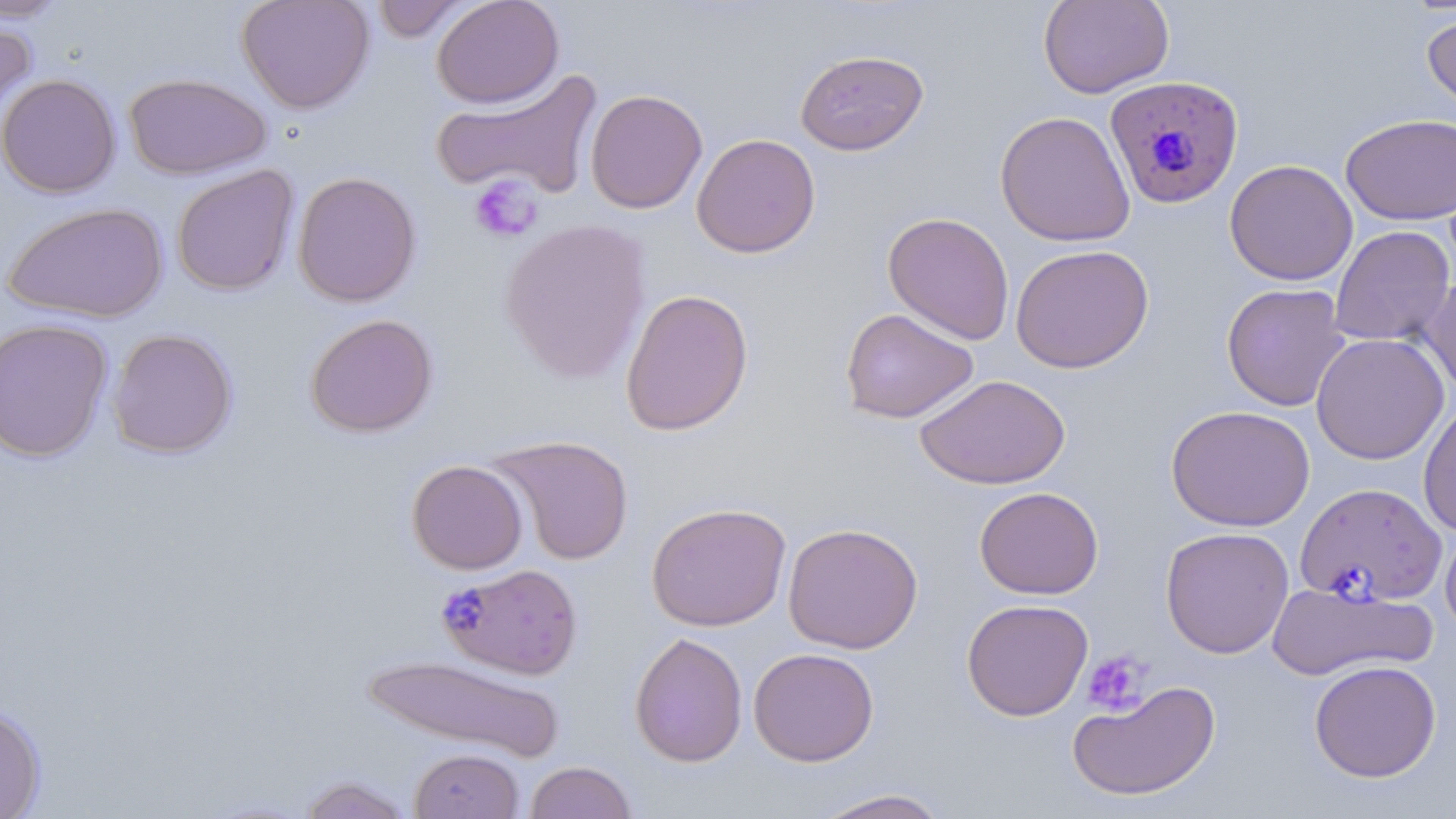
Approximate bounding boxes as (x1, y1, x2, y2) in pixels. Plasmodium falciparum-infected red blood cell locations: (1104, 75, 1244, 210), (1295, 481, 1447, 605), (437, 569, 579, 684). Platelet locations: (469, 173, 544, 244), (1082, 650, 1152, 716). Uninfected red blood cell locations: (0, 0, 71, 22), (237, 0, 375, 114), (370, 0, 473, 42), (431, 0, 564, 109), (1038, 0, 1174, 99), (1421, 11, 1456, 118), (0, 14, 37, 131), (795, 49, 929, 156), (432, 70, 603, 201), (123, 72, 272, 180), (0, 74, 121, 198), (585, 89, 708, 214), (994, 110, 1135, 247), (1340, 113, 1456, 225), (691, 133, 821, 258), (1224, 159, 1358, 286), (171, 165, 299, 297), (292, 170, 422, 308), (3, 201, 168, 323), (882, 211, 1015, 345), (499, 219, 653, 384), (1329, 225, 1455, 347), (1010, 244, 1155, 373), (1419, 275, 1456, 398), (1221, 282, 1351, 412), (620, 288, 754, 436), (839, 308, 978, 424), (305, 313, 438, 437), (0, 317, 114, 463), (107, 328, 238, 459), (1311, 332, 1450, 465), (915, 374, 1070, 490), (1418, 401, 1456, 538), (1166, 404, 1315, 532), (488, 434, 635, 565), (407, 459, 529, 575), (974, 487, 1104, 599), (646, 502, 791, 631), (783, 522, 923, 654), (1440, 523, 1456, 637), (1160, 526, 1294, 659), (1267, 580, 1437, 682), (961, 598, 1093, 721), (629, 632, 748, 767), (748, 647, 879, 767), (360, 652, 566, 762), (1308, 660, 1442, 783), (1067, 679, 1220, 802), (0, 702, 47, 819), (410, 748, 524, 819), (524, 761, 637, 819), (296, 775, 416, 819), (812, 788, 953, 818). Slide-level diagnosis: Plasmodium falciparum. Thin blood smear. Image is 1456×819 pixels. Single field of view. May-Grünwald-Giemsa-stained preparation. 1000x magnification. Optical microscopy.